Report the malaria status of this cell.
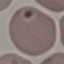
Uninfected.

capture = smartphone camera at the microscope eyepiece
stain = Giemsa
image type = automatically extracted cell patch, resized to 64 × 64 pixels
preparation = thin smear